State the preparation type.
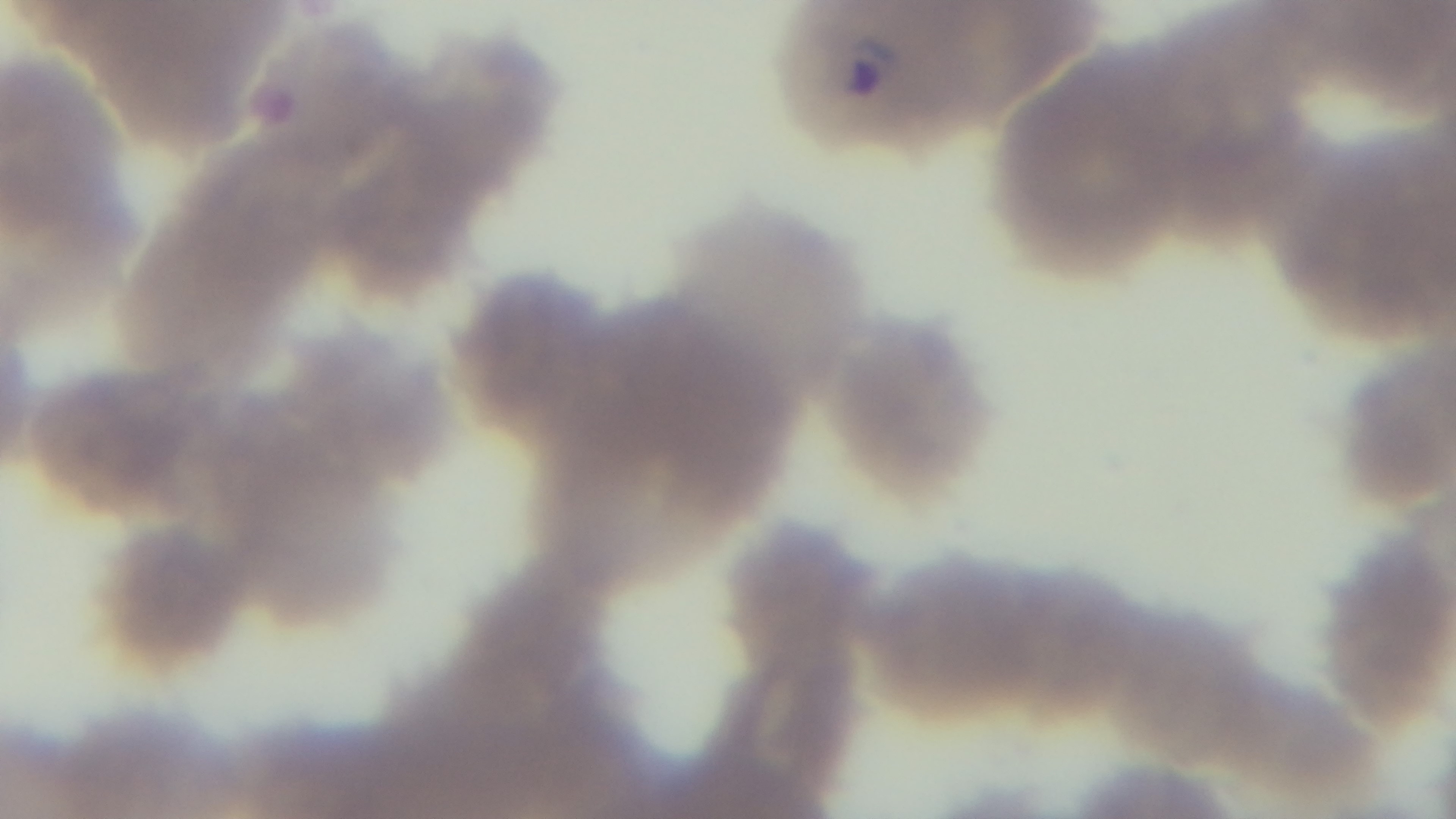
A thin smear.

Giemsa stain. Malaria status: infected. Light microscopy. Single field of view. Captured with a mounted 4K digital camera. 100x oil-immersion objective.